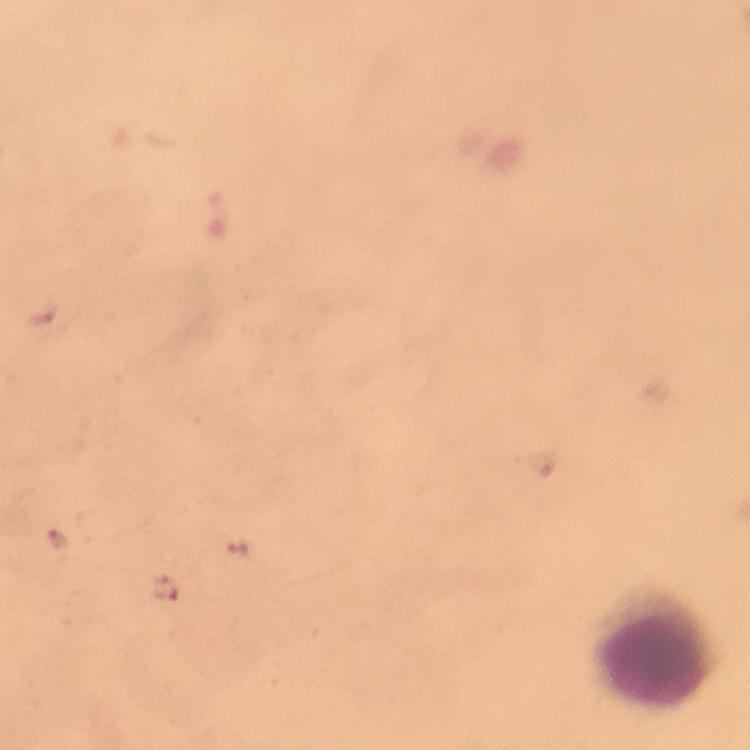
immersion oil = applied
stain = Giemsa
magnification = 100x
context = from a diagnostic examination for malaria
capture = smartphone photograph through a microscope
image size = 750×750 pixels
cropped from = one field of view
preparation = thick blood film
malaria parasite locations = approximate centers as [x, y] in pixels: [59, 536], [166, 589]
leukocyte locations = approximate centers as [x, y] in pixels: [656, 644]